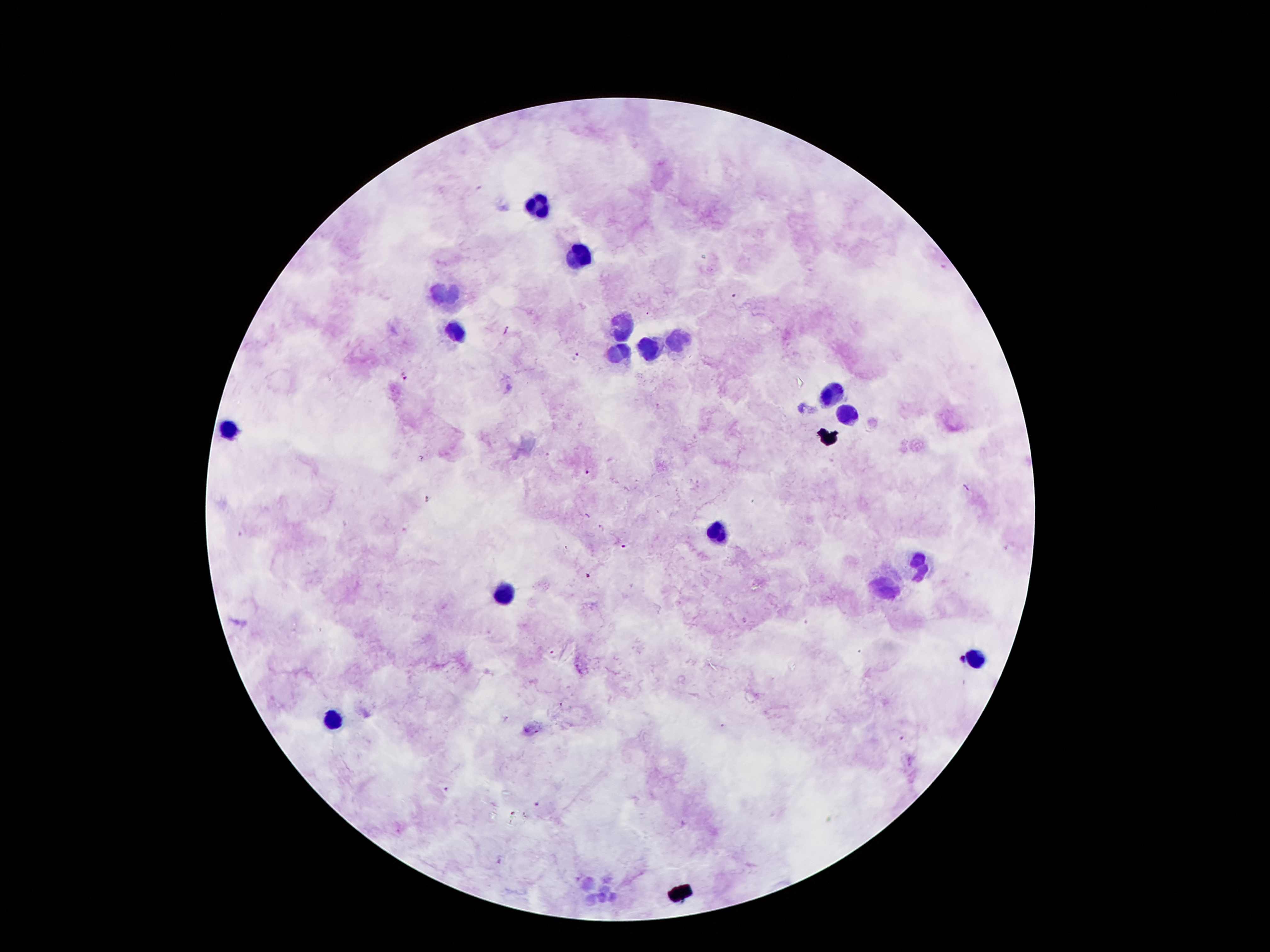

Approximate object centers, in pixels from the top-left corner.
Summary:
  - Leukocyte locations: (x=538, y=206), (x=577, y=256), (x=444, y=296), (x=621, y=327), (x=454, y=332), (x=679, y=341), (x=650, y=348), (x=619, y=349), (x=832, y=396), (x=847, y=411), (x=228, y=430), (x=719, y=532), (x=921, y=564), (x=884, y=585), (x=501, y=597), (x=975, y=658), (x=333, y=721), (x=599, y=890)
  - Plasmodium parasite locations: (x=732, y=294), (x=648, y=314), (x=508, y=330), (x=576, y=354), (x=405, y=377), (x=588, y=472), (x=967, y=488), (x=602, y=528), (x=623, y=546), (x=961, y=661), (x=723, y=727), (x=903, y=738), (x=444, y=789), (x=537, y=805)
  - Field of view: one from this slide
  - Preparation: thick blood film
  - Image size: 1270×952 pixels
  - Stain: Giemsa
  - Magnification: 100x
  - Capture: smartphone through the microscope eyepiece
  - Patient malaria status: infected with Plasmodium falciparum